Describe the morphology of the erythrocytes.
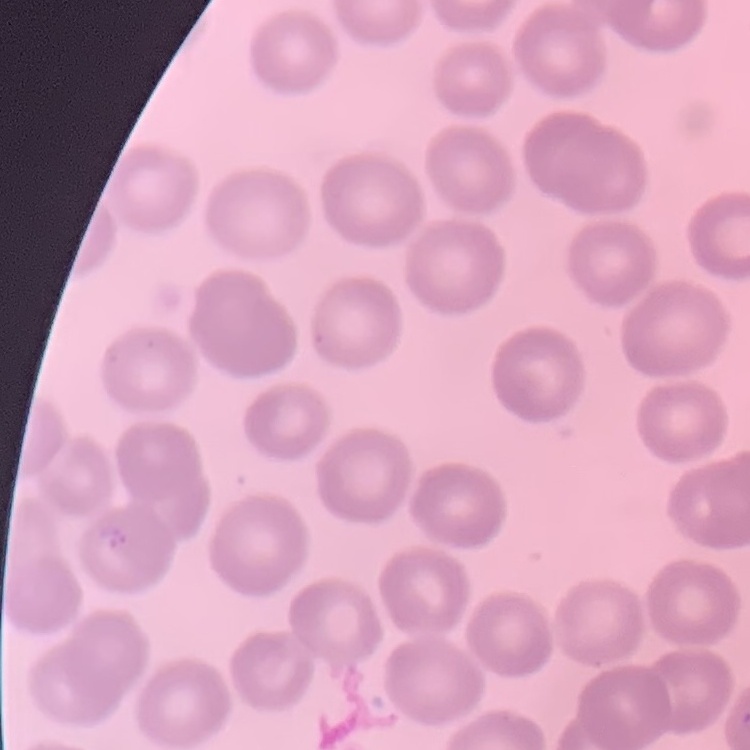
They show no rouleaux formation.

Summary:
  - Image type: square crop of a larger photomicrograph
  - Stain: Field's or Giemsa
  - Preparation: thin blood smear